Report the malaria status of this cell.
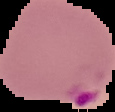
It is parasitized.

Segmented cell region on a black background. From a thin blood film. Image is 115×112 pixels.